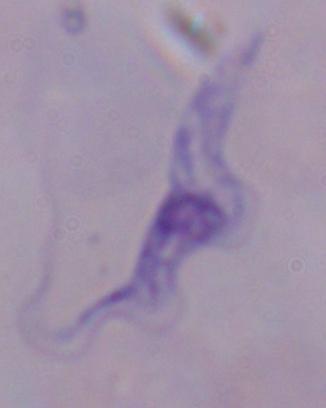
Summary:
  - Magnification: 1000x
  - Modality: micrograph
  - Identification: trypanosome